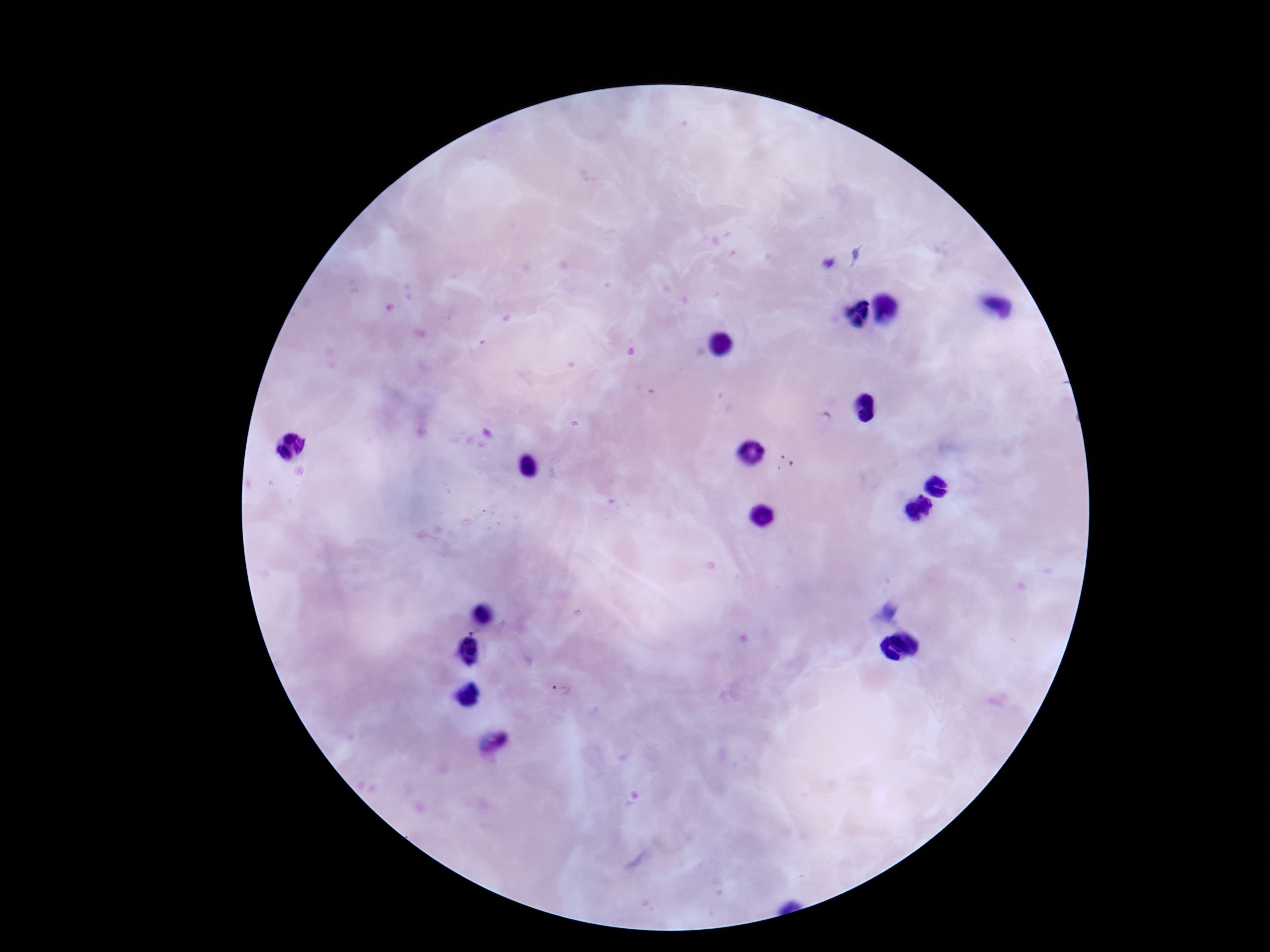
Approximate centers as [x, y] in pixels. Plasmodium parasite locations: [785, 462], [567, 691]. Smartphone photograph taken through the microscope eyepiece. Giemsa-stained preparation. 100x magnification. Patient malaria status: infected. One field from this slide. Image is 1270×952 pixels. Thick blood film.